Describe the morphology of the red blood cells.
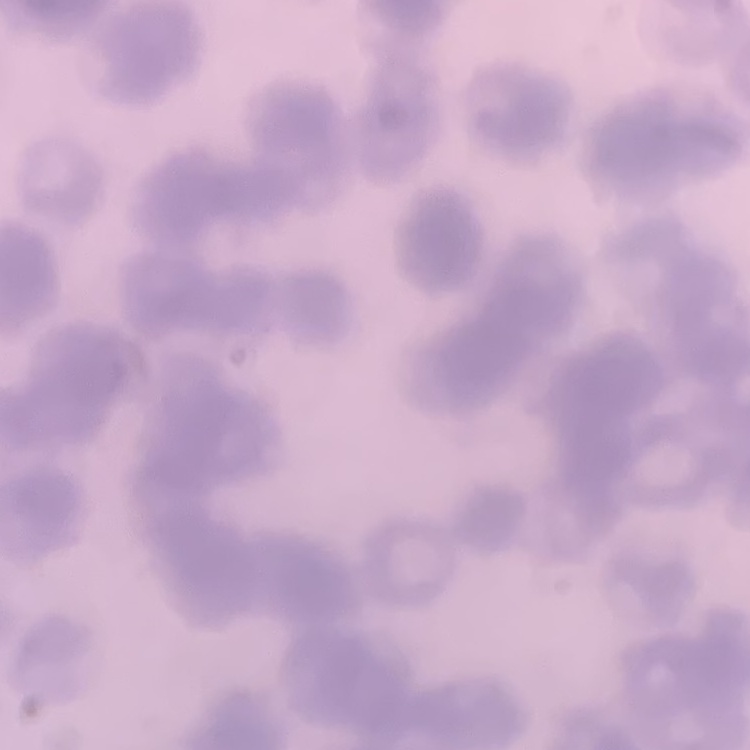
They show rouleaux formation.

Thin blood film. Square crop of a larger photomicrograph. Field's or Giemsa stain.